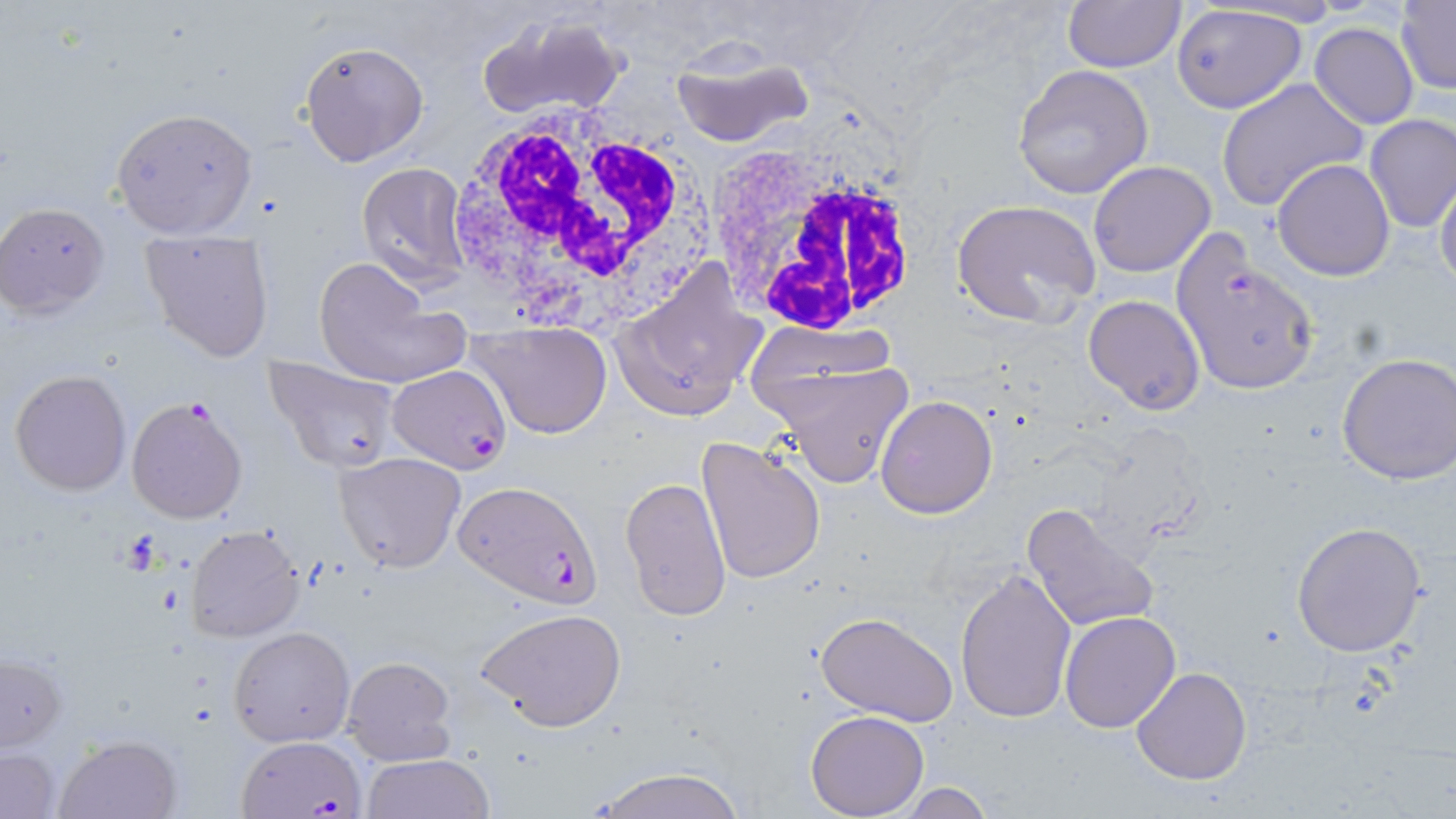
Summary:
  - Coordinate format: approximate bounding boxes as named x1/y1/x2/y2 corners in pixels
  - White blood cell locations: (x1=444, y1=108, x2=705, y2=325), (x1=704, y1=143, x2=926, y2=340)
  - Plasmodium falciparum-infected red blood cell locations: (x1=1167, y1=230, x2=1319, y2=395), (x1=388, y1=364, x2=509, y2=474), (x1=126, y1=396, x2=248, y2=523), (x1=452, y1=478, x2=602, y2=609), (x1=237, y1=734, x2=368, y2=819)
  - Uninfected red blood cell locations: (x1=1060, y1=0, x2=1186, y2=72), (x1=1396, y1=0, x2=1456, y2=93), (x1=1170, y1=3, x2=1307, y2=113), (x1=474, y1=11, x2=629, y2=123), (x1=1309, y1=22, x2=1420, y2=130), (x1=299, y1=41, x2=429, y2=166), (x1=668, y1=49, x2=814, y2=150), (x1=1012, y1=64, x2=1153, y2=199), (x1=1218, y1=79, x2=1369, y2=212), (x1=111, y1=107, x2=258, y2=238), (x1=1364, y1=113, x2=1456, y2=232), (x1=1272, y1=158, x2=1395, y2=281), (x1=1087, y1=161, x2=1216, y2=277), (x1=356, y1=163, x2=472, y2=288), (x1=1435, y1=170, x2=1456, y2=293), (x1=951, y1=199, x2=1102, y2=326), (x1=2, y1=203, x2=110, y2=316), (x1=139, y1=227, x2=277, y2=364), (x1=312, y1=258, x2=469, y2=392), (x1=614, y1=259, x2=768, y2=421), (x1=1084, y1=294, x2=1206, y2=415), (x1=473, y1=320, x2=612, y2=439), (x1=756, y1=350, x2=915, y2=489), (x1=1335, y1=352, x2=1456, y2=486), (x1=264, y1=355, x2=402, y2=474), (x1=9, y1=369, x2=131, y2=495), (x1=875, y1=395, x2=998, y2=519), (x1=695, y1=435, x2=826, y2=586), (x1=334, y1=452, x2=468, y2=574), (x1=620, y1=476, x2=733, y2=623), (x1=1021, y1=501, x2=1161, y2=635), (x1=1290, y1=521, x2=1428, y2=658), (x1=187, y1=526, x2=306, y2=642), (x1=952, y1=566, x2=1077, y2=725), (x1=476, y1=607, x2=627, y2=733), (x1=814, y1=610, x2=957, y2=726), (x1=1060, y1=610, x2=1183, y2=733), (x1=229, y1=626, x2=355, y2=747), (x1=1, y1=653, x2=65, y2=751), (x1=340, y1=655, x2=455, y2=767), (x1=1132, y1=666, x2=1251, y2=786), (x1=805, y1=710, x2=929, y2=817), (x1=54, y1=734, x2=184, y2=819), (x1=1, y1=746, x2=61, y2=819), (x1=361, y1=754, x2=497, y2=818), (x1=581, y1=768, x2=748, y2=819), (x1=895, y1=782, x2=996, y2=818)
  - Platelet locations: (x1=119, y1=532, x2=164, y2=570)
  - Slide-level diagnosis: Plasmodium falciparum
  - Stain: May-Grünwald-Giemsa
  - Image size: 1456×819 pixels
  - Field of view: single
  - Preparation: thin blood smear
  - Modality: light microscopy
  - Magnification: 1000x